Comment on the morphology of the erythrocytes.
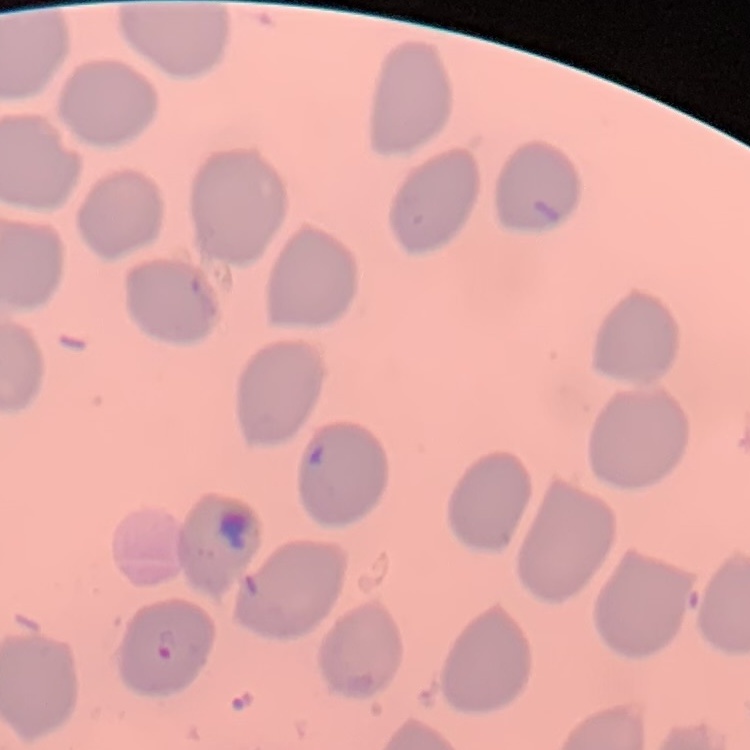
They show no rouleaux formation.

Summary:
  - Image type: one tile cut from a larger photomicrograph
  - Stain: Field's or Giemsa
  - Preparation: thin blood film